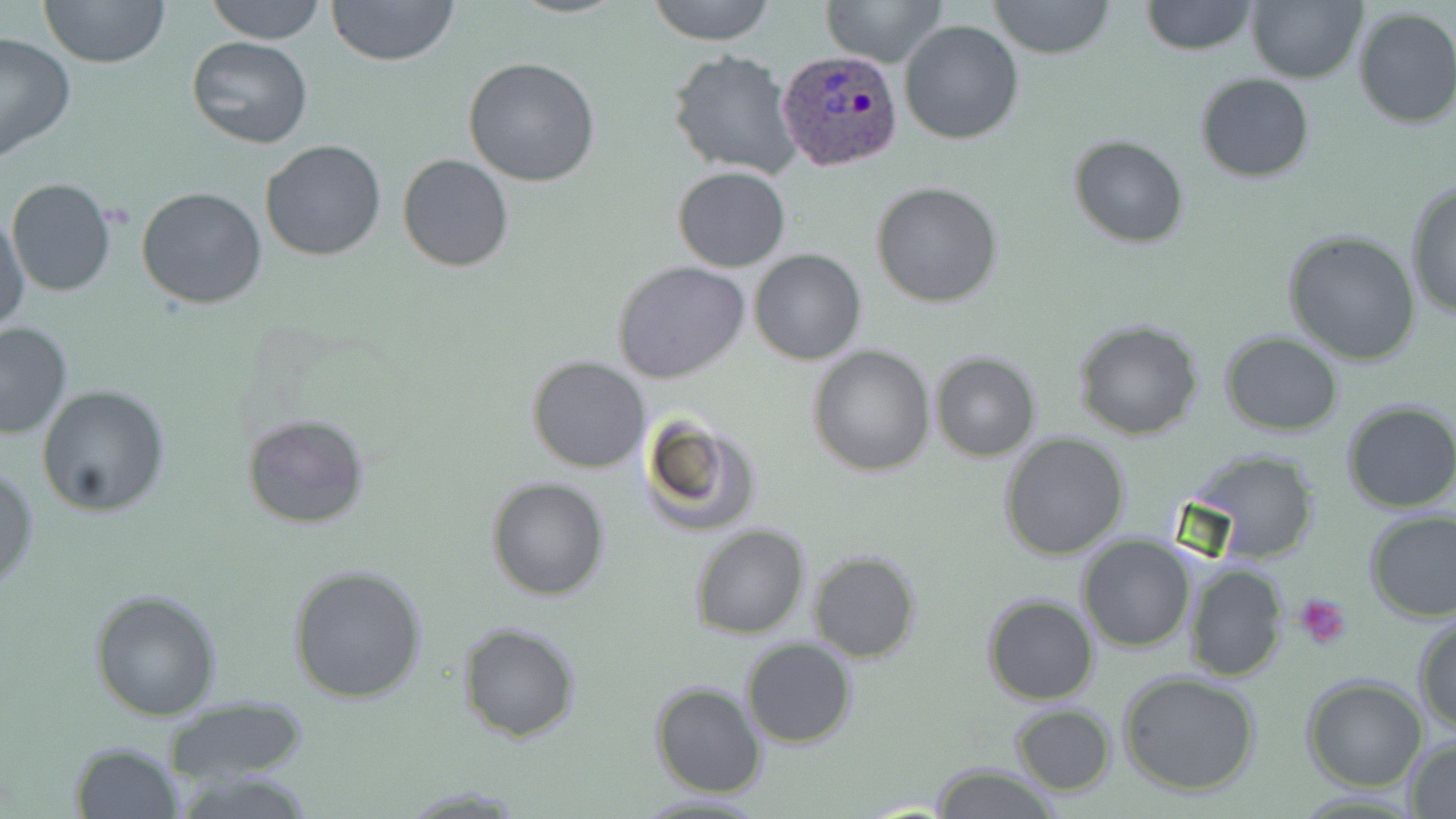
Summary:
  - Coordinate format: approximate bounding boxes as (x1, y1, x2, y2) in pixels
  - Platelet locations: (1294, 593, 1352, 650)
  - Uninfected red blood cell locations: (39, 0, 170, 70), (204, 0, 328, 44), (326, 0, 460, 68), (645, 0, 777, 45), (823, 0, 946, 68), (987, 0, 1115, 59), (1246, 0, 1365, 84), (1141, 1, 1258, 55), (1351, 6, 1456, 129), (898, 19, 1023, 144), (0, 31, 75, 164), (185, 37, 314, 151), (668, 49, 802, 178), (462, 57, 600, 187), (1195, 74, 1316, 183), (1068, 135, 1188, 247), (260, 138, 385, 261), (397, 154, 516, 272), (672, 167, 790, 272), (7, 178, 116, 296), (871, 181, 1003, 307), (1405, 182, 1456, 324), (136, 186, 267, 309), (1, 212, 29, 329), (1283, 229, 1423, 365), (749, 248, 867, 365), (612, 262, 751, 384), (1071, 317, 1205, 441), (0, 322, 73, 441), (1219, 330, 1344, 436), (807, 346, 935, 477), (930, 351, 1042, 461), (527, 356, 651, 474), (37, 385, 170, 518), (1340, 399, 1456, 515), (637, 413, 760, 540), (241, 415, 371, 530), (999, 434, 1130, 559), (1190, 450, 1323, 564), (0, 466, 38, 589), (486, 476, 611, 601), (1363, 508, 1456, 623), (688, 525, 811, 640), (1078, 536, 1197, 654), (807, 551, 922, 662), (1181, 561, 1288, 682), (286, 564, 427, 705), (89, 588, 223, 720), (982, 595, 1099, 706), (1413, 616, 1456, 735), (458, 622, 581, 742), (741, 639, 855, 749), (1117, 670, 1262, 796), (1302, 676, 1428, 791), (650, 680, 768, 798), (166, 696, 308, 786), (1010, 703, 1115, 795), (1402, 736, 1456, 817), (70, 741, 184, 819), (930, 763, 1058, 819), (399, 784, 531, 815), (630, 791, 771, 818)
  - Plasmodium ovale-infected red blood cell locations: (777, 50, 904, 173)
  - Slide-level diagnosis: Plasmodium ovale
  - Stain: May-Grünwald-Giemsa
  - Modality: optical microscopy
  - Image size: 1456×819 pixels
  - Preparation: thin blood smear
  - Magnification: 1000x
  - Field of view: one of a larger specimen